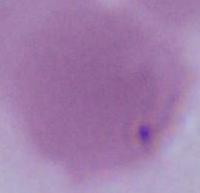
Summary:
  - Modality: micrograph
  - Identification: red blood cell
  - Magnification: 1000x